Report the malaria status of this cell.
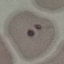
Parasitized.

{
  "capture": "smartphone camera at the microscope eyepiece",
  "preparation": "thin blood film",
  "image_type": "cell patch, automatically extracted from a larger field of view and resized to 64 × 64 pixels",
  "stain": "Giemsa"
}